Locate every Plasmodium ovale-infected red blood cell.
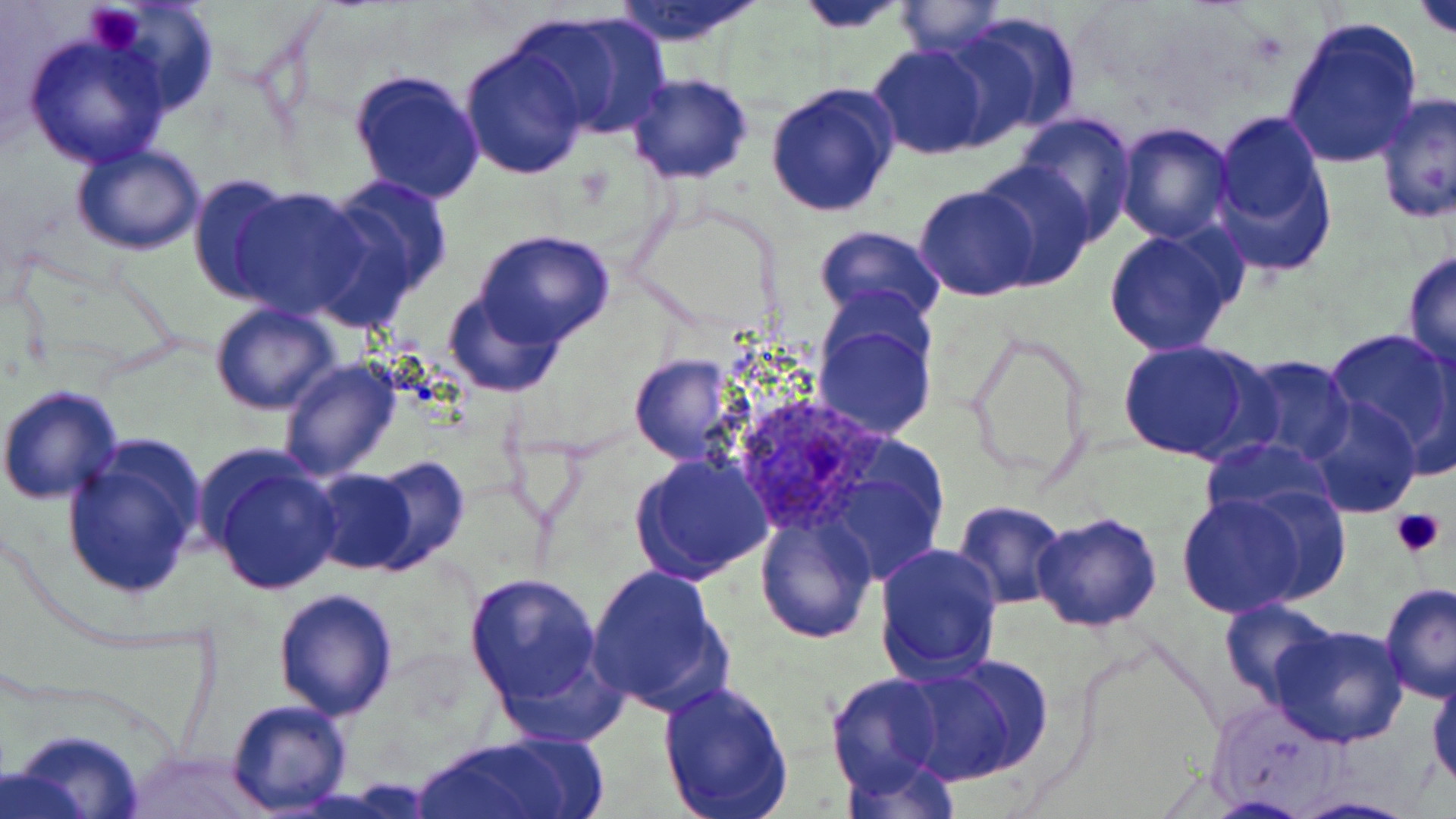

Approximate bounding boxes as (x1,y1)-(x2,y2) corner pairs in pixels.
Plasmodium ovale-infected red blood cells: (729,393)-(887,531).

Summary:
  - Platelet locations: (84,5)-(145,51), (1390,504)-(1447,559)
  - Uninfected red blood cell locations: (93,0)-(220,118), (791,0)-(916,31), (1410,0)-(1456,44), (607,1)-(769,47), (892,1)-(1007,56), (526,11)-(673,142), (947,12)-(1084,141), (1280,14)-(1424,171), (21,31)-(176,171), (458,43)-(591,179), (867,43)-(992,160), (348,68)-(487,205), (626,74)-(755,185), (763,82)-(899,216), (1374,92)-(1456,227), (1212,109)-(1335,270), (1014,113)-(1137,243), (1112,121)-(1234,244), (69,144)-(206,256), (969,159)-(1097,293), (186,174)-(300,303), (314,176)-(452,326), (914,184)-(1040,301), (225,187)-(374,320), (813,225)-(947,331), (1099,226)-(1245,359), (471,230)-(617,349), (1402,249)-(1456,370), (442,286)-(563,397), (209,303)-(343,416), (813,318)-(935,441), (1323,327)-(1456,464), (965,332)-(1091,482), (1413,336)-(1456,479), (1115,339)-(1268,464), (629,354)-(739,465), (1233,355)-(1357,465), (278,356)-(403,480), (0,384)-(124,504), (1305,398)-(1423,519), (60,435)-(208,603), (1197,436)-(1338,528), (820,445)-(952,590), (197,446)-(344,598), (629,451)-(775,584), (360,456)-(471,575), (306,462)-(430,576), (1175,488)-(1322,618), (949,500)-(1069,609), (1031,511)-(1163,633), (754,513)-(876,644), (873,542)-(1003,681), (585,564)-(733,716), (464,573)-(607,712), (1378,582)-(1456,701), (273,588)-(398,720), (1219,598)-(1342,706), (1267,624)-(1411,749), (905,656)-(1054,785), (1428,665)-(1456,793), (825,673)-(948,794), (656,678)-(793,818), (1205,697)-(1348,811), (224,700)-(354,816), (6,729)-(146,819), (412,737)-(579,818), (126,748)-(266,817), (835,750)-(959,818), (1287,795)-(1425,818)
  - Slide-level diagnosis: Plasmodium ovale
  - Modality: optical microscopy
  - Preparation: thin blood smear
  - Magnification: 1000x
  - Image size: 1456×819 pixels
  - Stain: May-Grünwald-Giemsa
  - Field of view: one of a larger specimen